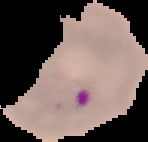 Image is 148×142 pixels. From a thin blood smear. Segmented cell region on a black background. Result: Plasmodium parasites identified.